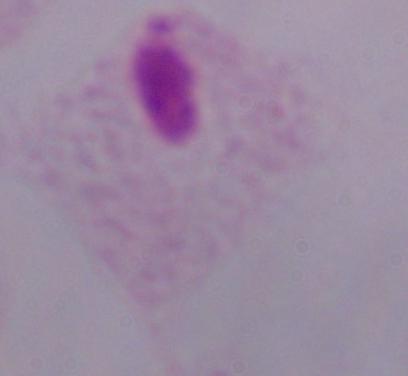

{
  "magnification": "1000x",
  "identification": "trichomonad",
  "modality": "micrograph"
}